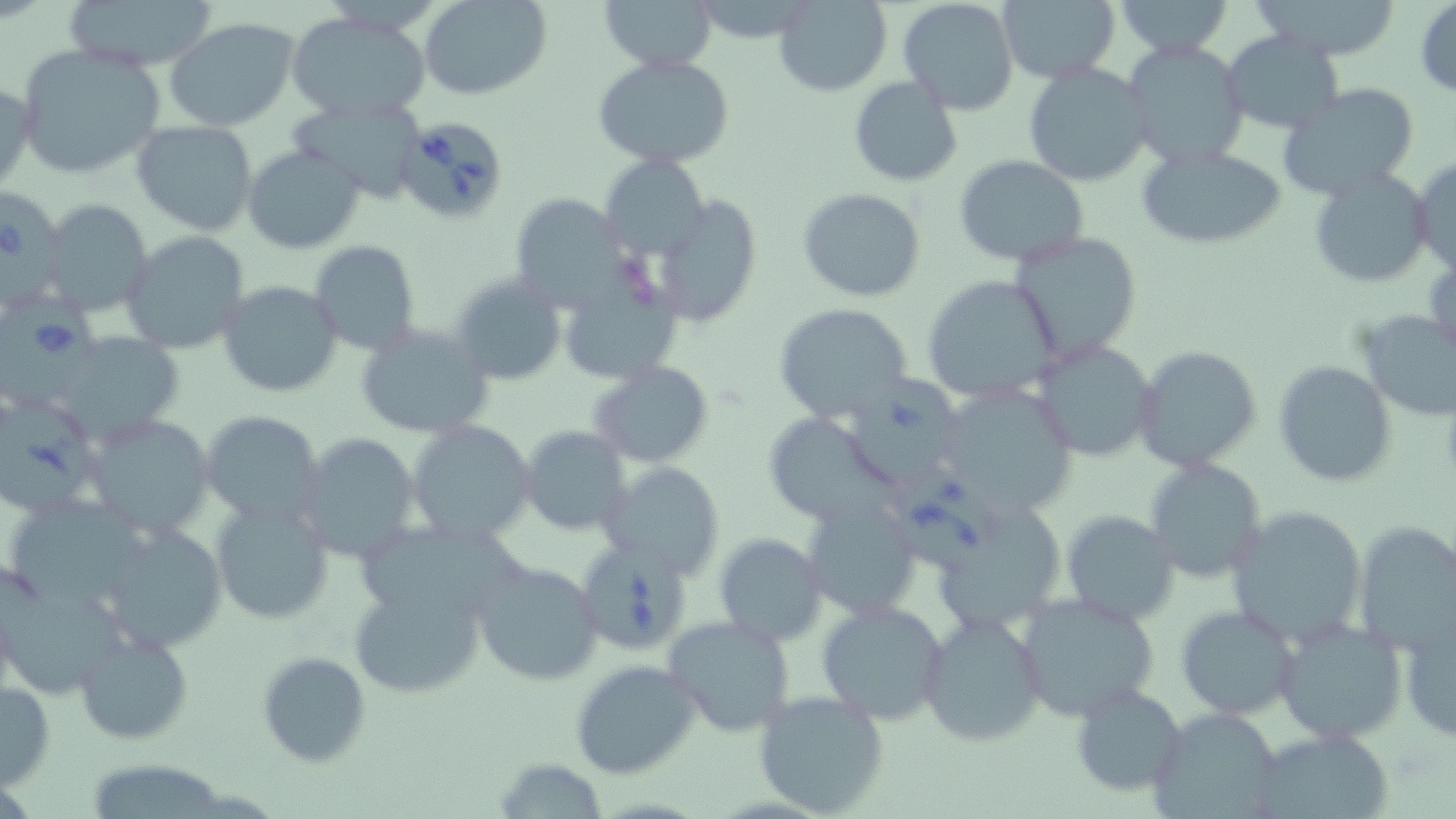

Summary:
  - Coordinate format: approximate bounding boxes as [x1, y1, x2, y2] in pixels
  - Uninfected red blood cell locations: [61, 0, 219, 72], [422, 0, 550, 99], [602, 0, 720, 69], [773, 0, 892, 97], [897, 0, 1018, 116], [996, 0, 1121, 85], [1112, 0, 1234, 59], [1254, 1, 1404, 60], [1414, 2, 1456, 98], [285, 11, 432, 120], [165, 19, 299, 131], [1222, 31, 1346, 135], [1125, 41, 1251, 171], [15, 43, 170, 183], [592, 54, 735, 168], [1023, 63, 1152, 187], [848, 76, 962, 187], [0, 80, 35, 194], [1274, 84, 1422, 202], [288, 95, 430, 200], [132, 120, 260, 236], [1135, 143, 1287, 250], [243, 144, 366, 255], [953, 154, 1089, 267], [601, 155, 709, 258], [1411, 155, 1456, 274], [1307, 167, 1431, 288], [797, 188, 926, 302], [655, 195, 762, 327], [513, 196, 640, 318], [39, 199, 152, 316], [120, 231, 251, 354], [1010, 232, 1144, 365], [309, 240, 424, 357], [448, 273, 568, 386], [921, 274, 1061, 405], [562, 279, 696, 378], [217, 280, 342, 398], [773, 302, 914, 423], [1353, 308, 1456, 422], [355, 323, 493, 441], [1031, 338, 1158, 462], [1132, 344, 1262, 473], [1272, 361, 1397, 487], [588, 362, 713, 467], [933, 384, 1080, 525], [199, 409, 326, 528], [765, 414, 893, 526], [86, 415, 215, 542], [404, 420, 536, 545], [519, 427, 630, 536], [295, 434, 420, 562], [1145, 458, 1268, 583], [604, 460, 725, 579], [209, 497, 333, 627], [803, 497, 921, 620], [13, 499, 157, 611], [1226, 505, 1366, 647], [1059, 510, 1178, 626], [351, 518, 552, 619], [97, 520, 233, 653], [1353, 521, 1456, 653], [715, 533, 828, 645], [472, 560, 602, 686], [348, 577, 487, 699], [2, 578, 125, 700], [1015, 594, 1161, 725], [815, 598, 950, 725], [1173, 605, 1301, 720], [918, 613, 1048, 747], [1401, 613, 1456, 746], [663, 616, 797, 740], [1271, 617, 1407, 747], [74, 628, 195, 746], [257, 651, 372, 767], [569, 659, 700, 779], [0, 680, 54, 791], [1068, 683, 1187, 801], [754, 689, 889, 817], [1148, 706, 1285, 818], [1249, 728, 1398, 819], [492, 758, 609, 818], [90, 764, 225, 819]
  - Babesia divergens-infected red blood cell locations: [397, 114, 509, 224], [0, 190, 68, 309], [0, 298, 106, 412], [850, 370, 965, 494], [1, 392, 103, 518], [885, 461, 1007, 574], [572, 539, 693, 658]
  - Slide-level diagnosis: Babesia divergens
  - Stain: May-Grünwald-Giemsa
  - Image size: 1456×819 pixels
  - Preparation: thin blood film
  - Magnification: 1000x
  - Modality: optical microscopy
  - Field of view: single